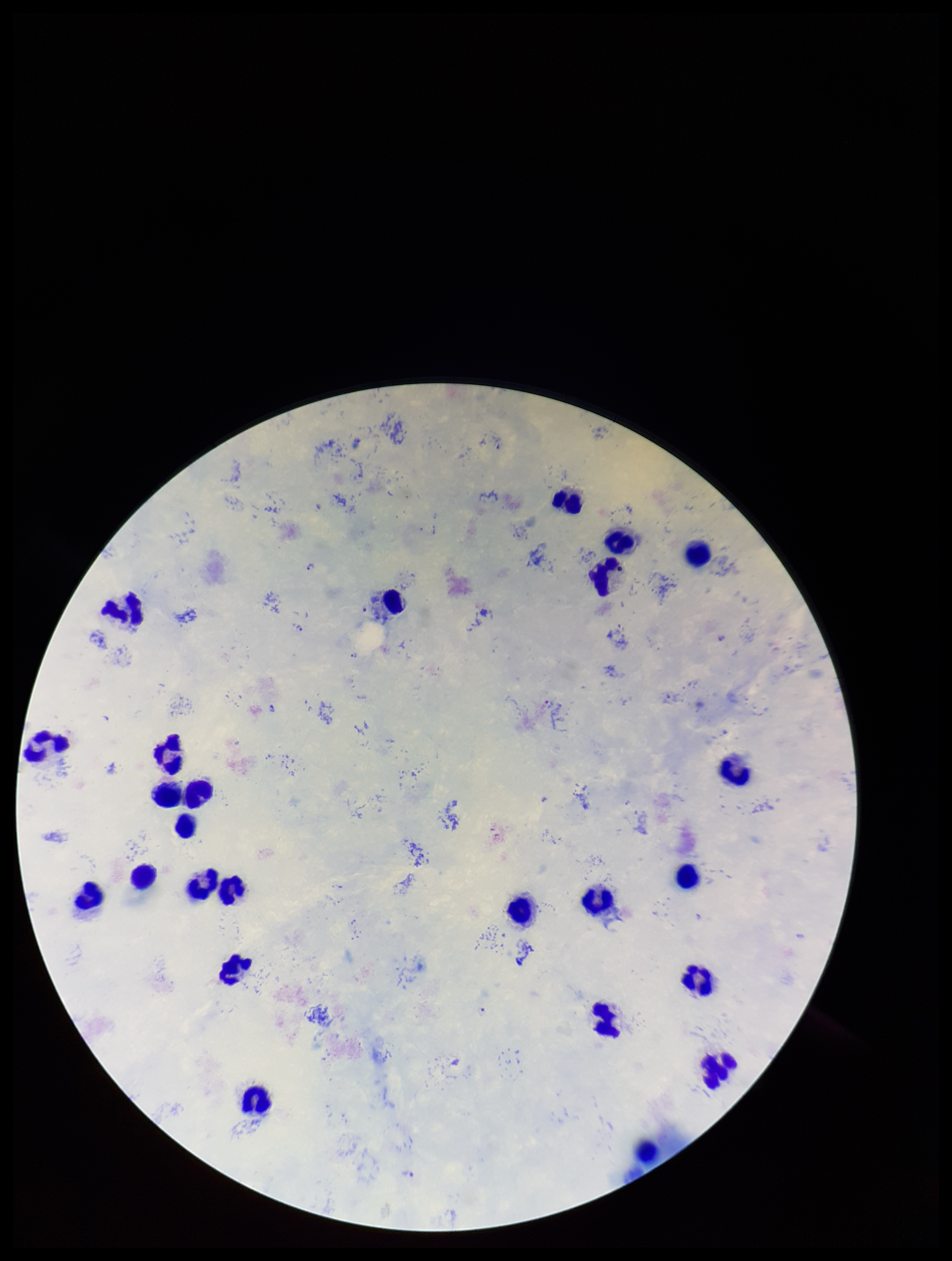
Summary:
  - Capture: smartphone photograph through the microscope eyepiece
  - Plasmodium parasites: detected
  - Patient malaria status: infected
  - Species reported for this patient: Plasmodium falciparum
  - Image size: 952×1261 pixels
  - Stain: Giemsa
  - Leukocyte count: 25
  - Preparation: thick blood smear
  - Parasite count: 6
  - Field of view: one from this slide